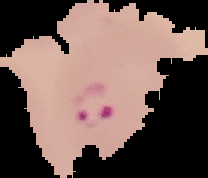
Summary:
  - Image size: 208×178 pixels
  - Result: Plasmodium parasites detected
  - Preparation: thin blood film
  - Image type: segmented cell region with the area outside set to black